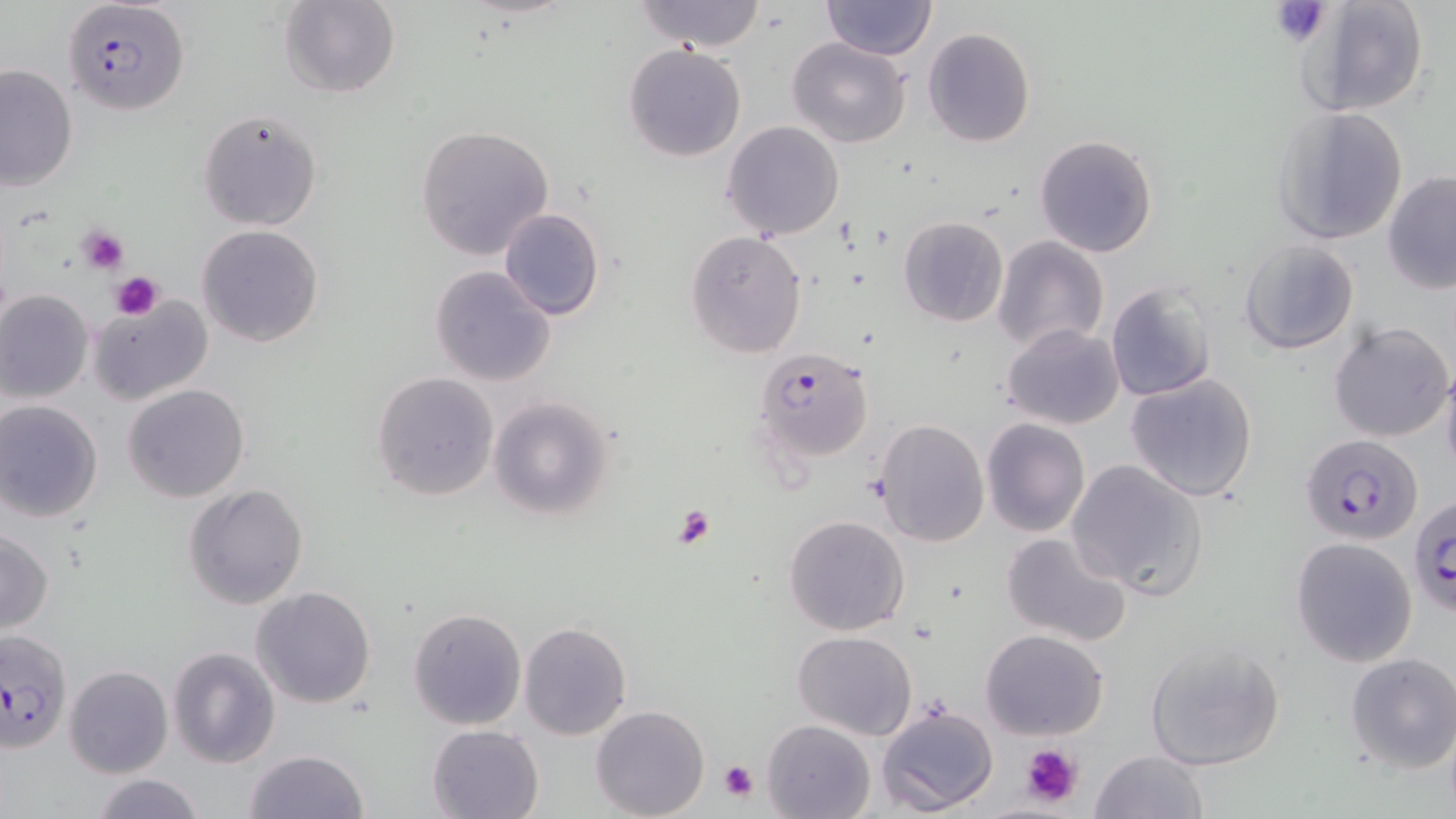

Summary:
  - Coordinate format: approximate bounding boxes as [x1, y1, x2, y2] in pixels
  - Uninfected red blood cell locations: [280, 0, 400, 99], [635, 0, 766, 51], [820, 0, 937, 61], [1295, 0, 1430, 116], [922, 27, 1035, 147], [786, 37, 911, 149], [623, 44, 748, 163], [0, 63, 78, 193], [1269, 106, 1410, 247], [197, 108, 324, 231], [721, 120, 846, 240], [415, 125, 556, 261], [1033, 133, 1160, 259], [1381, 171, 1456, 296], [498, 208, 605, 322], [898, 215, 1009, 327], [196, 225, 324, 348], [685, 230, 809, 359], [991, 235, 1109, 355], [1239, 239, 1360, 354], [430, 264, 557, 386], [1104, 281, 1217, 401], [0, 289, 94, 405], [88, 298, 214, 405], [1329, 320, 1453, 443], [1001, 323, 1124, 430], [1440, 365, 1456, 483], [371, 371, 498, 502], [1126, 371, 1260, 503], [123, 383, 250, 502], [487, 396, 618, 520], [0, 401, 104, 523], [980, 417, 1090, 538], [873, 418, 989, 547], [1065, 458, 1208, 601], [182, 482, 310, 610], [783, 514, 910, 636], [0, 529, 54, 634], [999, 530, 1134, 646], [1290, 537, 1418, 667], [250, 585, 377, 710], [408, 608, 526, 730], [519, 620, 632, 740], [979, 628, 1110, 741], [793, 630, 917, 741], [1144, 640, 1286, 770], [168, 647, 279, 767], [1344, 652, 1456, 775], [64, 665, 171, 778], [592, 704, 710, 818], [875, 705, 998, 816], [762, 718, 875, 819], [426, 724, 545, 818], [243, 749, 369, 819], [1089, 749, 1209, 819], [90, 775, 206, 819]
  - Platelet locations: [1270, 1, 1330, 47], [75, 226, 130, 275], [112, 272, 161, 316], [671, 503, 719, 549], [1020, 744, 1082, 809], [719, 759, 760, 802]
  - Plasmodium falciparum-infected red blood cell locations: [63, 1, 191, 116], [753, 347, 873, 461], [1300, 434, 1423, 547], [1409, 497, 1456, 621], [0, 629, 74, 752]
  - Slide-level diagnosis: Plasmodium falciparum
  - Modality: light microscopy
  - Preparation: thin blood smear
  - Stain: May-Grünwald-Giemsa
  - Magnification: 1000x
  - Field of view: one of a larger specimen
  - Image size: 1456×819 pixels